Identify the blood parasite species.
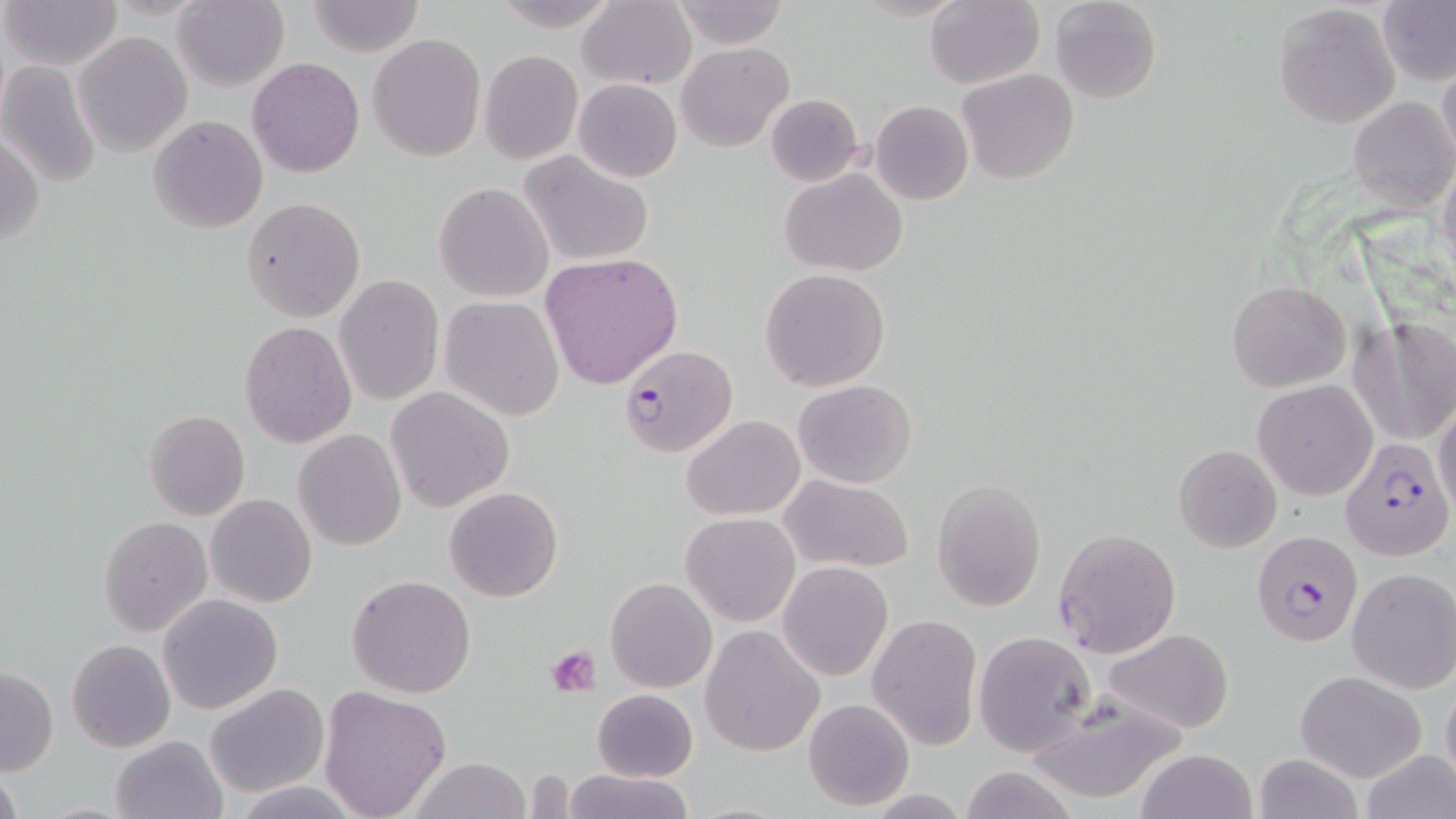

Plasmodium falciparum.

Approximate bounding boxes as (x1, y1, x2, y2) in pixels. Plasmodium falciparum-infected red blood cell locations: (617, 344, 738, 458), (1340, 436, 1453, 562), (1251, 529, 1363, 649). Platelet locations: (549, 645, 600, 696). Uninfected red blood cell locations: (1, 0, 123, 71), (172, 0, 289, 91), (493, 0, 620, 31), (669, 0, 789, 49), (1050, 0, 1162, 104), (308, 1, 424, 56), (577, 1, 696, 89), (924, 1, 1045, 88), (1377, 1, 1456, 87), (1272, 3, 1401, 130), (74, 32, 191, 156), (368, 33, 486, 161), (677, 41, 793, 151), (479, 49, 584, 166), (1438, 53, 1456, 168), (247, 58, 364, 177), (0, 62, 102, 190), (958, 69, 1078, 185), (573, 78, 682, 182), (765, 93, 865, 187), (1348, 98, 1456, 209), (870, 101, 974, 206), (148, 115, 269, 235), (1, 126, 45, 250), (518, 149, 655, 269), (1436, 159, 1456, 287), (781, 169, 908, 276), (433, 182, 554, 303), (242, 198, 364, 321), (539, 254, 683, 391), (759, 268, 891, 391), (334, 275, 444, 408), (1227, 281, 1350, 391), (440, 297, 565, 421), (1362, 318, 1456, 445), (239, 321, 358, 448), (793, 379, 916, 489), (1253, 379, 1378, 501), (385, 386, 514, 511), (1433, 402, 1456, 521), (142, 409, 250, 521), (681, 415, 804, 520), (293, 429, 407, 550), (1172, 444, 1282, 553), (780, 476, 913, 573), (932, 479, 1048, 611), (444, 486, 563, 602), (206, 494, 317, 607), (681, 512, 800, 626), (98, 516, 213, 637), (1052, 527, 1182, 659), (777, 562, 893, 682), (1347, 568, 1456, 694), (345, 574, 477, 698), (605, 577, 717, 693), (158, 593, 283, 714), (865, 613, 982, 750), (699, 624, 825, 758), (1102, 627, 1235, 734), (972, 630, 1097, 757), (67, 639, 175, 752), (2, 667, 58, 775), (1295, 670, 1427, 782), (1440, 680, 1456, 789), (205, 683, 329, 798), (318, 685, 453, 819), (591, 689, 697, 782), (1022, 691, 1187, 805), (803, 698, 915, 812), (110, 735, 227, 819), (1135, 748, 1257, 819), (1359, 748, 1456, 819), (1254, 751, 1362, 819), (410, 757, 530, 819), (0, 765, 24, 819), (957, 767, 1079, 819), (561, 768, 695, 819), (235, 781, 362, 817). 1000x magnification. May-Grünwald-Giemsa stain. One field of a larger specimen. Light microscopy. Thin blood smear. Image is 1456×819 pixels.